Describe the morphology of the erythrocytes.
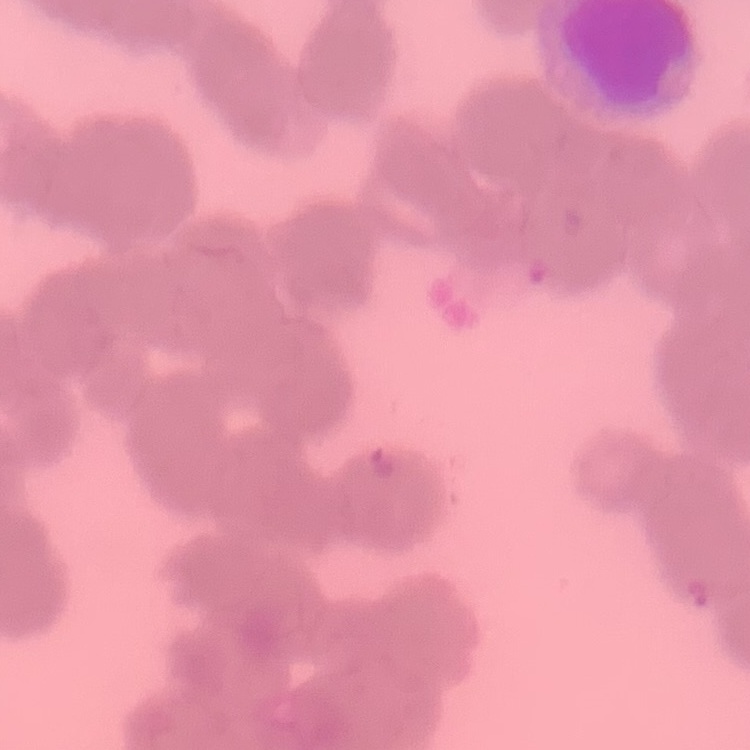
They show rouleaux formation.

Square crop of a larger photomicrograph. Thin blood film. Field's or Giemsa stain.